State which parasite is depicted.
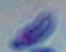

Toxoplasma gondii.

{
  "magnification": "1000x",
  "modality": "photomicrograph"
}